Report the malaria status of this cell.
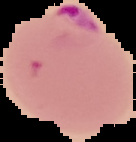

Parasitized.

Summary:
  - Preparation: thin blood film
  - Image type: segmented cell region with the area outside set to black
  - Image size: 136×142 pixels